Classify this cell by malaria status.
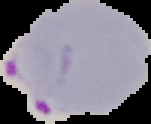

Parasitized.

Segmented cell region on a black background. From a thin blood film. Image is 151×124 pixels.